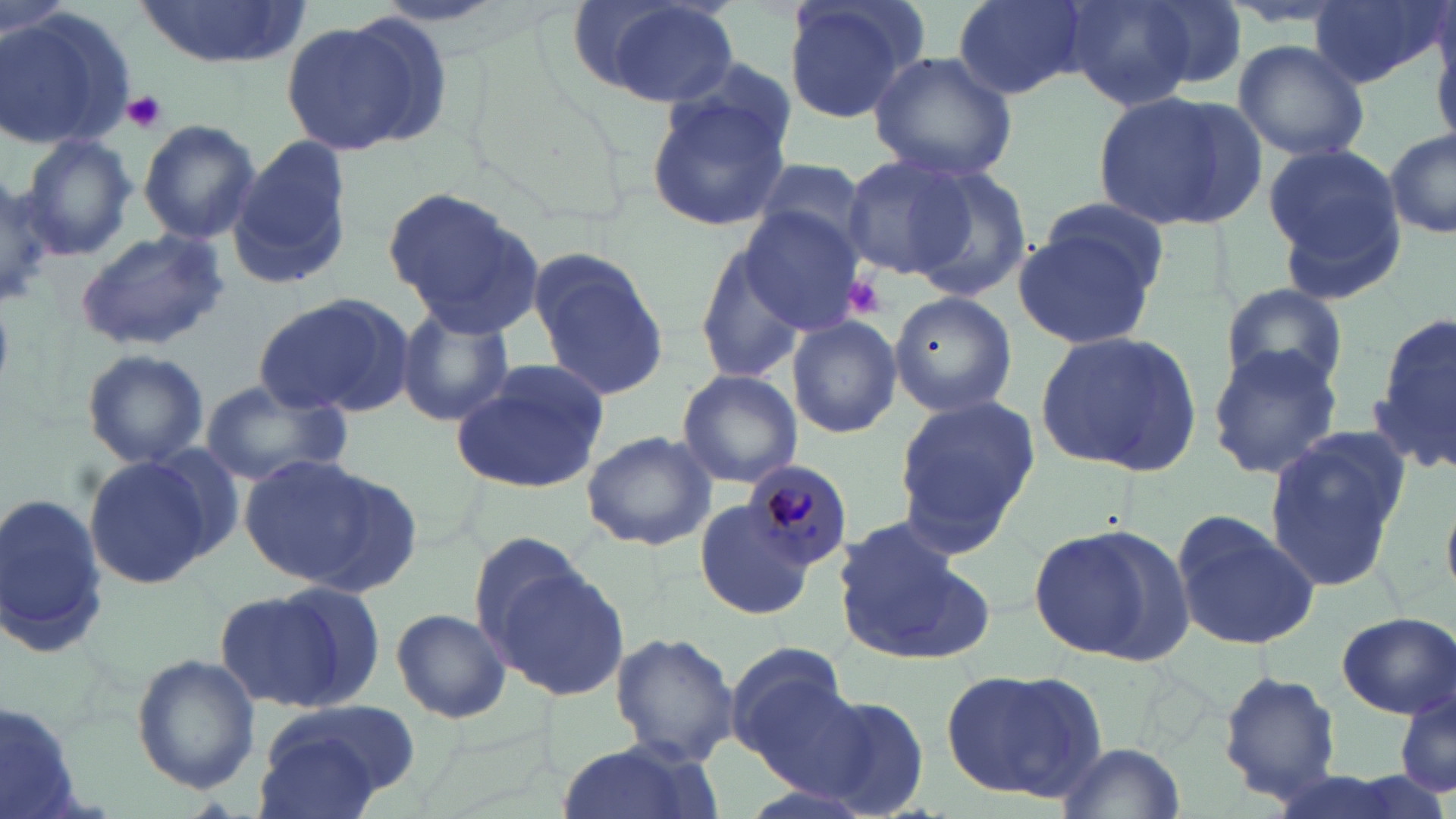

Summary:
  - Coordinate format: approximate bounding boxes as named x1/y1/x2/y2 corners in pixels
  - Uninfected red blood cell locations: (x1=129, y1=0, x2=311, y2=68), (x1=577, y1=0, x2=739, y2=110), (x1=778, y1=0, x2=925, y2=126), (x1=954, y1=0, x2=1088, y2=99), (x1=1063, y1=0, x2=1212, y2=111), (x1=1134, y1=0, x2=1250, y2=95), (x1=1309, y1=0, x2=1446, y2=89), (x1=0, y1=8, x2=135, y2=150), (x1=1430, y1=17, x2=1456, y2=149), (x1=276, y1=18, x2=428, y2=159), (x1=1233, y1=39, x2=1371, y2=165), (x1=865, y1=49, x2=1018, y2=183), (x1=646, y1=90, x2=794, y2=233), (x1=1092, y1=90, x2=1261, y2=228), (x1=138, y1=119, x2=261, y2=245), (x1=1385, y1=129, x2=1456, y2=239), (x1=19, y1=133, x2=139, y2=261), (x1=229, y1=138, x2=357, y2=287), (x1=1261, y1=141, x2=1407, y2=290), (x1=839, y1=153, x2=978, y2=282), (x1=748, y1=155, x2=872, y2=258), (x1=903, y1=162, x2=1033, y2=303), (x1=0, y1=180, x2=62, y2=307), (x1=382, y1=185, x2=545, y2=335), (x1=1036, y1=199, x2=1170, y2=296), (x1=735, y1=207, x2=866, y2=332), (x1=1011, y1=213, x2=1163, y2=353), (x1=75, y1=229, x2=229, y2=352), (x1=692, y1=238, x2=812, y2=385), (x1=531, y1=250, x2=669, y2=403), (x1=1220, y1=282, x2=1348, y2=396), (x1=889, y1=290, x2=1019, y2=418), (x1=253, y1=292, x2=413, y2=419), (x1=395, y1=304, x2=516, y2=429), (x1=1373, y1=312, x2=1454, y2=475), (x1=787, y1=314, x2=902, y2=439), (x1=1033, y1=326, x2=1204, y2=477), (x1=1206, y1=345, x2=1343, y2=482), (x1=81, y1=349, x2=210, y2=467), (x1=451, y1=362, x2=613, y2=493), (x1=675, y1=370, x2=803, y2=489), (x1=200, y1=380, x2=354, y2=488), (x1=890, y1=394, x2=1041, y2=554), (x1=1263, y1=429, x2=1412, y2=591), (x1=580, y1=430, x2=717, y2=549), (x1=141, y1=443, x2=249, y2=561), (x1=83, y1=453, x2=219, y2=588), (x1=237, y1=454, x2=384, y2=586), (x1=298, y1=468, x2=425, y2=596), (x1=0, y1=493, x2=109, y2=657), (x1=694, y1=501, x2=816, y2=621), (x1=1171, y1=511, x2=1321, y2=650), (x1=832, y1=520, x2=984, y2=664), (x1=1028, y1=525, x2=1192, y2=664), (x1=466, y1=531, x2=594, y2=662), (x1=486, y1=561, x2=630, y2=702), (x1=212, y1=587, x2=356, y2=712), (x1=389, y1=606, x2=512, y2=723), (x1=1336, y1=613, x2=1455, y2=717), (x1=611, y1=633, x2=740, y2=766), (x1=723, y1=642, x2=855, y2=773), (x1=130, y1=654, x2=260, y2=796), (x1=939, y1=666, x2=1109, y2=804), (x1=1219, y1=671, x2=1343, y2=802), (x1=1395, y1=690, x2=1455, y2=801), (x1=802, y1=691, x2=933, y2=815), (x1=0, y1=702, x2=88, y2=819), (x1=251, y1=703, x2=415, y2=816), (x1=560, y1=738, x2=714, y2=819), (x1=1057, y1=739, x2=1186, y2=819)
  - Plasmodium malariae-infected red blood cell locations: (x1=740, y1=459, x2=856, y2=573)
  - Platelet locations: (x1=123, y1=91, x2=167, y2=133), (x1=839, y1=274, x2=888, y2=317)
  - Slide-level diagnosis: Plasmodium malariae
  - Modality: optical microscopy
  - Preparation: thin blood smear
  - Image size: 1456×819 pixels
  - Field of view: single
  - Stain: May-Grünwald-Giemsa
  - Magnification: 1000x